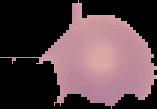
Image is 157×109 pixels. Malaria status: uninfected. From a thin blood film. Segmented cell region on a black background.